Describe the morphology of the erythrocytes.
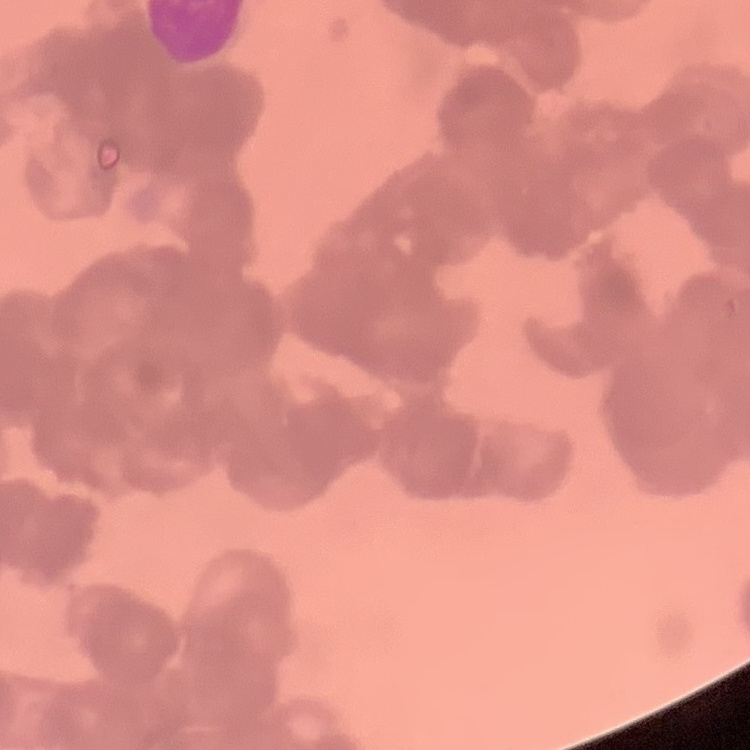
They show rouleaux formation.

Thin peripheral smear. Stained with either Field's or Giemsa. Square crop of a larger photomicrograph.